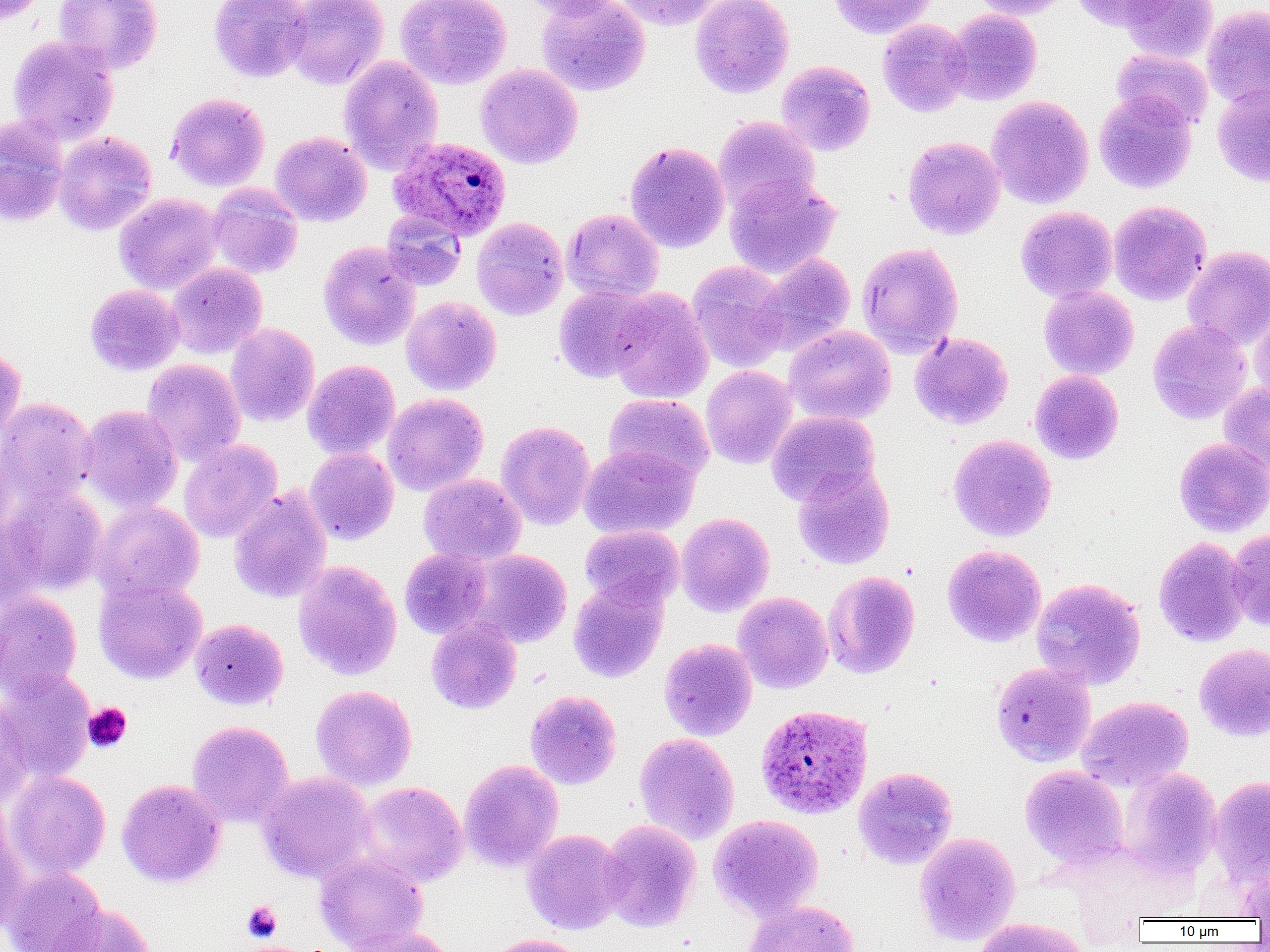
Summary:
  - Coordinate format: approximate bounding boxes as (x1, y1, x2, y2) in pixels
  - Platelet locations: (83, 703, 132, 753), (242, 902, 282, 942)
  - Plasmodium ovale-infected red blood cell locations: (388, 135, 511, 241), (755, 704, 873, 819)
  - Uninfected red blood cell locations: (0, 0, 46, 26), (54, 0, 162, 75), (209, 0, 312, 83), (285, 0, 388, 91), (395, 0, 512, 90), (518, 0, 624, 20), (536, 0, 650, 96), (612, 0, 719, 30), (690, 0, 794, 98), (828, 0, 936, 39), (969, 0, 1075, 19), (1072, 0, 1172, 31), (1119, 0, 1219, 63), (1202, 5, 1270, 109), (945, 9, 1042, 105), (878, 19, 972, 117), (8, 36, 118, 145), (1111, 49, 1214, 130), (339, 55, 444, 175), (776, 61, 875, 157), (475, 64, 583, 169), (1212, 85, 1270, 187), (1094, 90, 1197, 193), (165, 92, 270, 192), (986, 95, 1094, 209), (713, 116, 820, 214), (0, 117, 68, 226), (53, 131, 157, 235), (270, 131, 371, 227), (903, 136, 1005, 240), (625, 141, 730, 252), (724, 173, 841, 278), (207, 183, 304, 280), (114, 193, 224, 294), (1108, 201, 1211, 305), (1015, 206, 1118, 302), (562, 208, 664, 302), (381, 210, 467, 291), (471, 217, 568, 320), (318, 241, 421, 351), (856, 242, 963, 358), (1183, 246, 1270, 350), (752, 253, 856, 356), (687, 261, 790, 372), (167, 263, 267, 359), (84, 284, 184, 376), (553, 285, 656, 382), (1039, 285, 1139, 380), (607, 288, 713, 405), (401, 296, 501, 396), (1250, 305, 1270, 405), (1148, 320, 1252, 424), (225, 323, 320, 427), (784, 325, 896, 425), (909, 331, 1014, 430), (0, 346, 26, 443), (142, 359, 246, 467), (302, 359, 400, 460), (700, 365, 798, 469), (1030, 370, 1124, 465), (1219, 383, 1270, 480), (382, 393, 489, 496), (603, 393, 714, 485), (0, 398, 96, 506), (76, 404, 183, 513), (767, 410, 879, 506), (496, 421, 596, 530), (948, 434, 1057, 542), (0, 435, 16, 543), (1174, 438, 1270, 537), (179, 440, 282, 543), (579, 445, 698, 540), (305, 447, 399, 545), (793, 464, 895, 570), (419, 474, 526, 566), (3, 483, 107, 596), (228, 486, 332, 604), (90, 500, 204, 603), (676, 512, 774, 617), (0, 517, 48, 611), (580, 525, 684, 609), (1226, 528, 1270, 630), (1153, 536, 1250, 647), (942, 545, 1046, 647), (399, 548, 492, 639), (468, 549, 572, 648), (293, 560, 402, 681), (822, 570, 920, 679), (93, 576, 207, 684), (1031, 578, 1146, 690), (568, 581, 668, 683), (0, 591, 82, 699), (733, 592, 834, 693), (426, 617, 522, 714), (190, 618, 289, 710), (659, 639, 757, 741), (1194, 644, 1270, 742), (991, 662, 1096, 766), (0, 671, 95, 784), (311, 685, 417, 790), (524, 690, 622, 790), (1, 696, 33, 807), (1077, 696, 1193, 791), (187, 720, 294, 828), (634, 733, 740, 845), (459, 759, 564, 872), (1020, 765, 1129, 870), (853, 767, 958, 869), (1120, 768, 1222, 881), (5, 770, 111, 879), (257, 771, 376, 883), (1209, 775, 1270, 887), (117, 779, 226, 888), (356, 782, 468, 887), (708, 814, 823, 921), (0, 819, 29, 934), (598, 819, 701, 933), (523, 829, 626, 934), (914, 832, 1020, 946), (315, 852, 428, 952), (1238, 865, 1270, 920), (1, 866, 105, 952), (743, 900, 859, 952), (46, 904, 156, 952), (973, 918, 1089, 952), (343, 926, 457, 952), (482, 933, 589, 952)
  - Slide-level diagnosis: Plasmodium ovale
  - Preparation: thin blood smear
  - Field of view: one of a larger specimen
  - Modality: light microscopy
  - Image size: 1270×952 pixels
  - Magnification: 1000x